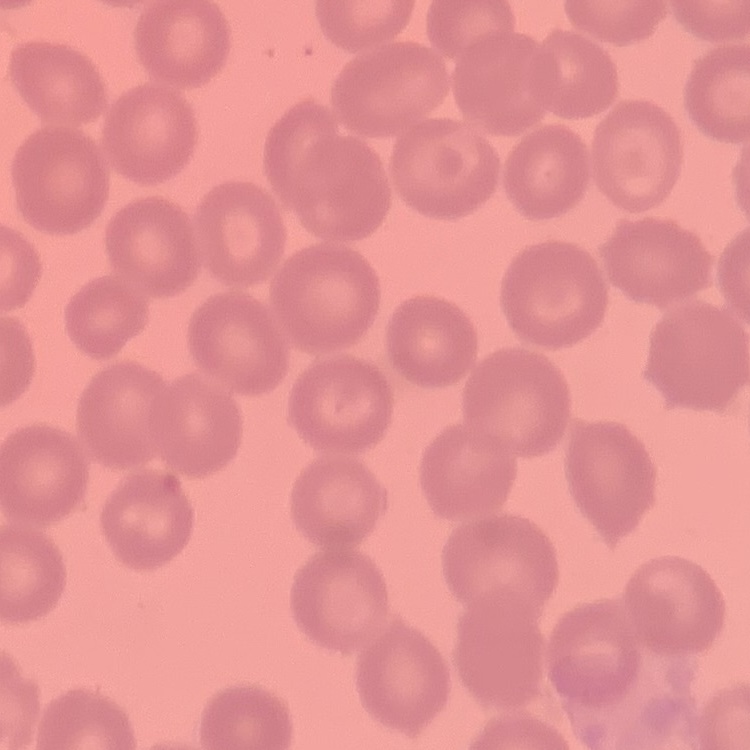

Summary:
  - Erythrocyte morphology: no rouleaux formation
  - Image type: square crop of a larger photomicrograph
  - Preparation: thin blood film
  - Stain: Field's or Giemsa